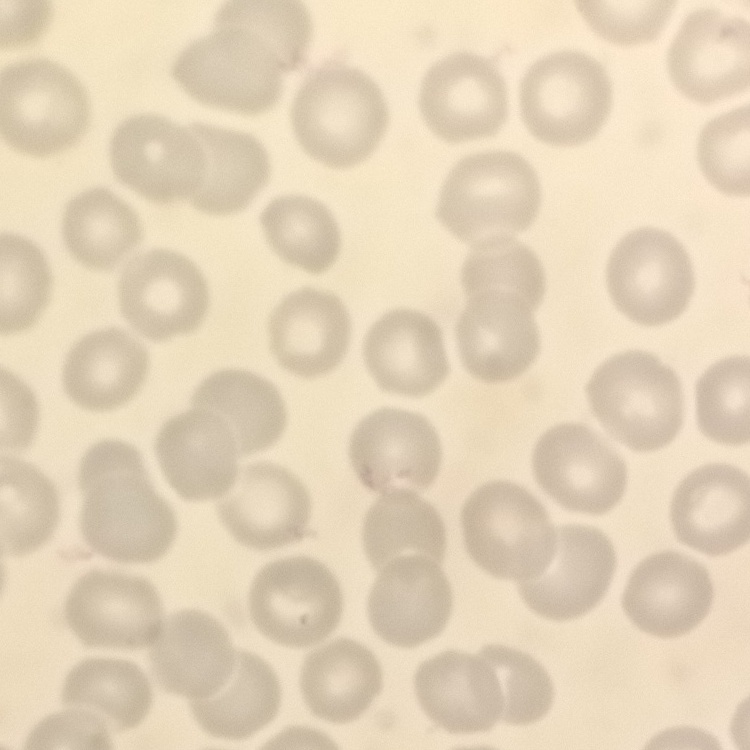

The erythrocytes exhibit no rouleaux formation. Square crop of a larger photomicrograph. Field's or Giemsa stain. Thin blood film.